Give the position of every malaria parasite and every leukocyte.
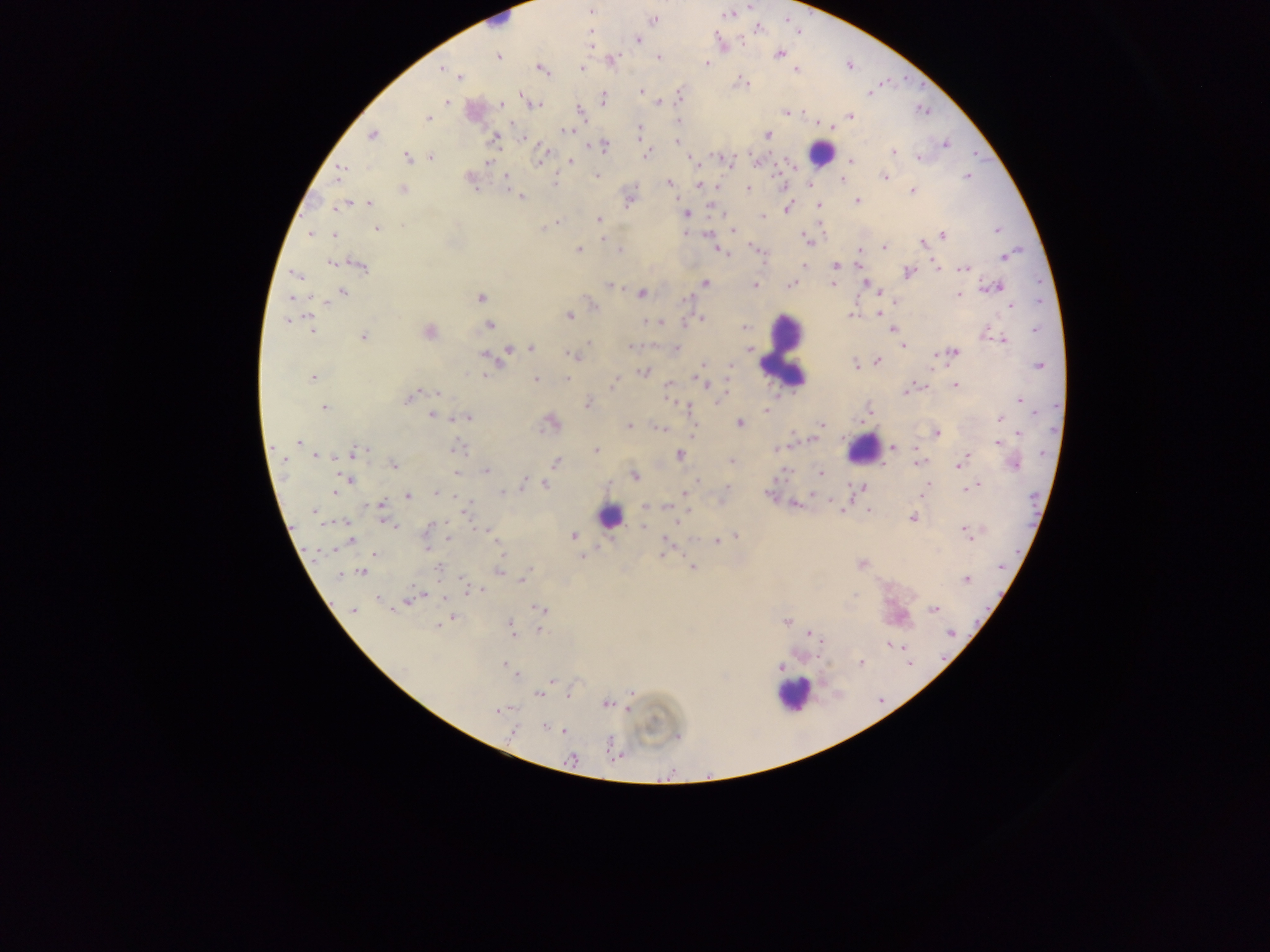
Approximate centers as x y in pixels.
Malaria parasites: 591 11; 653 20; 638 39; 591 43; 779 53; 496 57; 656 58; 610 60; 706 62; 850 66; 441 68; 541 68; 581 68; 796 69; 458 76; 745 83; 640 90; 868 92; 520 94; 680 95; 602 98; 447 101; 659 101; 535 104; 502 105; 580 112; 786 112; 850 115; 428 118; 678 122; 512 123; 819 124; 828 127; 638 129; 567 131; 372 134; 768 135; 494 138; 523 139; 677 139; 603 145; 945 145; 892 152; 646 154; 407 157; 432 157; 917 157; 690 158; 539 159; 756 160; 727 161; 570 162; 850 162; 488 163; 695 163; 339 171; 598 176; 505 177; 884 177; 966 177; 841 179; 471 182; 669 183; 699 185; 808 186; 716 187; 748 188; 402 189; 912 190; 520 196; 857 200; 629 201; 354 203; 367 203; 819 204; 343 205; 711 206; 786 208; 686 214; 762 217; 598 219; 820 227; 377 228; 997 230; 734 231; 311 233; 686 233; 706 233; 333 235; 941 235; 805 237; 809 241; 922 242; 755 247; 883 248; 578 249; 619 249; 717 250; 860 252; 1005 256; 333 262; 858 263; 836 265; 935 265; 360 266; 804 266; 963 269; 907 272; 295 274; 704 283; 832 283; 791 284; 609 285; 754 285; 995 287; 873 289; 343 291; 641 293; 878 293; 957 296; 480 297; 686 301; 896 301; 592 304; 1012 305; 484 310; 877 314; 567 315; 851 315; 701 318; 289 319; 662 321; 648 322; 489 325; 311 328; 743 328; 892 328; 1035 329; 428 331; 984 333; 362 335; 1003 339; 590 343; 901 345; 630 347; 531 349; 677 349; 750 349; 508 350; 953 352; 499 353; 484 354; 934 354; 572 356; 877 360; 703 363; 856 364; 1039 365; 643 372; 485 374; 694 376; 312 377; 699 378; 727 378; 536 379; 566 379; 613 383; 707 384; 667 385; 954 385; 726 389; 906 390; 415 393; 438 393; 409 398; 723 398; 1019 399; 586 403; 684 405; 322 407; 765 410; 432 415; 466 417; 1000 419; 862 422; 550 423; 739 423; 820 424; 629 426; 660 427; 936 433; 1018 434; 813 439; 298 441; 997 442; 789 445; 893 448; 915 448; 454 449; 774 449; 597 450; 351 453; 679 454; 315 455; 966 455; 555 462; 732 462; 917 463; 1014 463; 393 464; 959 465; 487 471; 455 472; 820 473; 634 476; 348 480; 524 481; 544 484; 979 485; 969 486; 726 487; 861 488; 963 488; 334 490; 437 492; 922 492; 685 493; 769 494; 814 494; 407 495; 794 504; 381 505; 646 506; 842 509; 314 510; 869 510; 466 511; 680 516; 912 517; 343 522; 388 522; 391 525; 644 527; 964 528; 488 529; 735 535; 573 536; 450 537; 349 540; 717 542; 666 546; 426 547; 663 552; 374 554; 582 557; 861 564; 692 566; 1000 568; 439 569; 529 569; 363 572; 499 572; 338 576; 966 579; 521 582; 479 590; 376 598; 409 599; 391 608; 540 609; 935 609; 353 611; 451 617; 787 621; 446 622; 440 624; 509 624; 539 631; 511 633; 808 633; 949 633; 820 640; 886 644; 902 645; 860 662; 504 663; 780 668; 517 675; 552 680; 566 693; 631 693; 538 694; 606 704; 628 709; 499 710; 543 726; 564 731; 512 732; 617 757; 572 759.
Leukocytes: 498 18; 819 153; 782 351; 863 449; 609 516; 794 693.

country = Ghana
preparation = thick blood film
image size = 1270×952 pixels
field of view = single
capture = mobile-phone photograph through a microscope